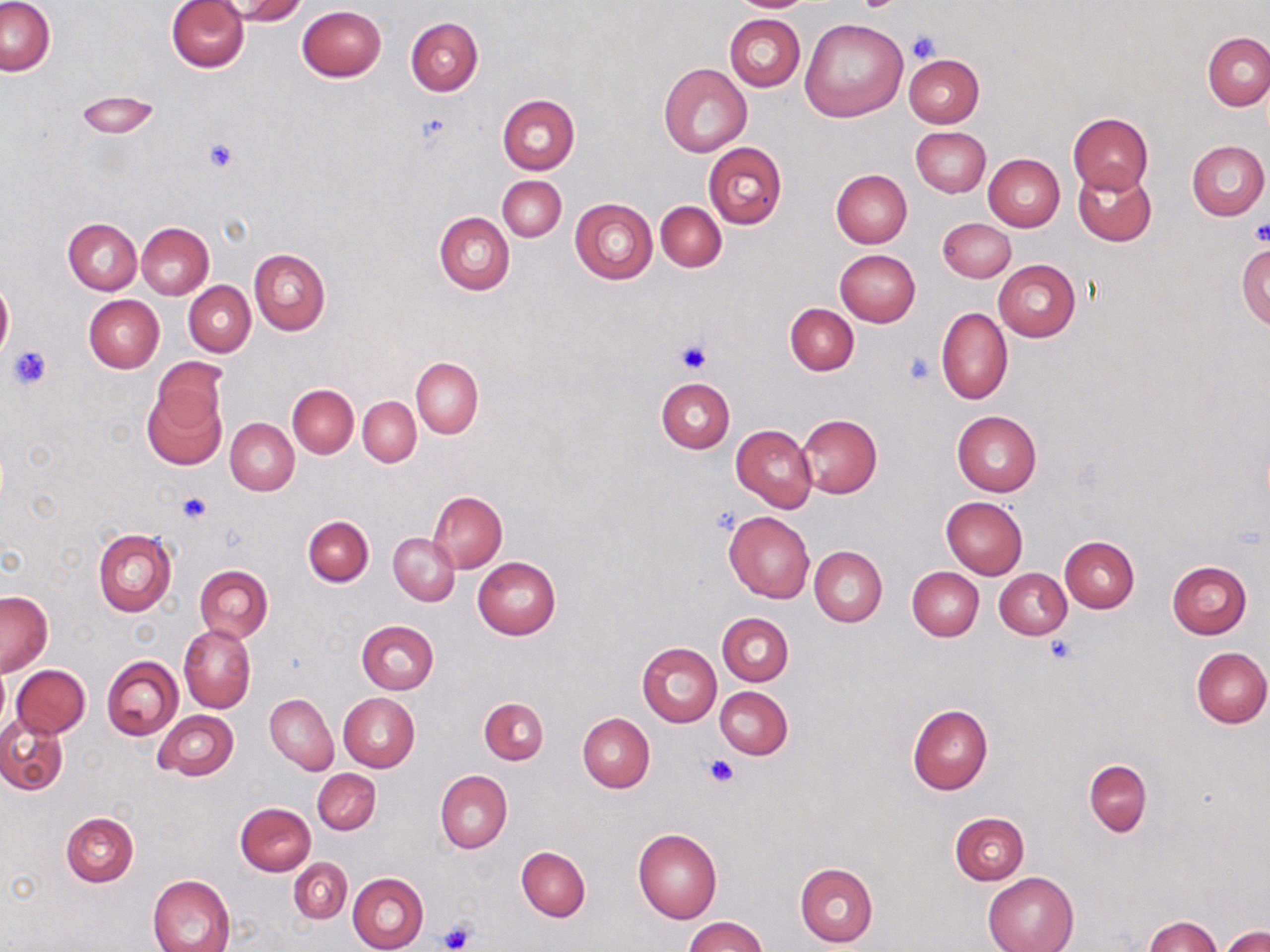
slide-level diagnosis = no evidence of blood parasites
stain = May-Grünwald-Giemsa
platelet locations = approximate bounding boxes as named x1/y1/x2/y2 corners in pixels: (x1=854, y1=0, x2=900, y2=12), (x1=908, y1=30, x2=938, y2=63), (x1=415, y1=111, x2=454, y2=148), (x1=204, y1=138, x2=238, y2=173), (x1=1249, y1=222, x2=1270, y2=248), (x1=675, y1=340, x2=712, y2=375), (x1=7, y1=345, x2=52, y2=391), (x1=903, y1=352, x2=936, y2=386), (x1=177, y1=491, x2=212, y2=526), (x1=1045, y1=636, x2=1078, y2=664), (x1=705, y1=756, x2=738, y2=788), (x1=438, y1=923, x2=476, y2=951)
modality = optical microscopy
uninfected red blood cell locations = approximate bounding boxes as named x1/y1/x2/y2 corners in pixels: (x1=167, y1=0, x2=249, y2=72), (x1=227, y1=0, x2=306, y2=24), (x1=730, y1=0, x2=814, y2=11), (x1=1, y1=1, x2=55, y2=76), (x1=298, y1=5, x2=387, y2=81), (x1=726, y1=14, x2=805, y2=90), (x1=405, y1=17, x2=482, y2=95), (x1=799, y1=17, x2=907, y2=122), (x1=1203, y1=32, x2=1270, y2=111), (x1=903, y1=53, x2=984, y2=127), (x1=658, y1=63, x2=751, y2=156), (x1=75, y1=90, x2=161, y2=139), (x1=496, y1=94, x2=580, y2=174), (x1=1069, y1=113, x2=1153, y2=194), (x1=910, y1=127, x2=989, y2=197), (x1=1186, y1=140, x2=1268, y2=220), (x1=703, y1=142, x2=786, y2=229), (x1=984, y1=154, x2=1064, y2=231), (x1=1073, y1=168, x2=1156, y2=247), (x1=831, y1=169, x2=912, y2=248), (x1=498, y1=176, x2=565, y2=242), (x1=570, y1=199, x2=658, y2=284), (x1=656, y1=202, x2=726, y2=270), (x1=434, y1=211, x2=514, y2=295), (x1=64, y1=218, x2=141, y2=295), (x1=938, y1=218, x2=1015, y2=281), (x1=136, y1=223, x2=213, y2=299), (x1=1238, y1=244, x2=1270, y2=327), (x1=250, y1=248, x2=330, y2=335), (x1=834, y1=249, x2=919, y2=328), (x1=993, y1=259, x2=1080, y2=341), (x1=0, y1=280, x2=13, y2=357), (x1=184, y1=282, x2=255, y2=356), (x1=83, y1=295, x2=164, y2=373), (x1=785, y1=304, x2=858, y2=375), (x1=936, y1=307, x2=1012, y2=405), (x1=412, y1=358, x2=482, y2=438), (x1=144, y1=374, x2=227, y2=467), (x1=655, y1=378, x2=734, y2=453), (x1=287, y1=384, x2=359, y2=458), (x1=358, y1=397, x2=420, y2=467), (x1=952, y1=411, x2=1041, y2=496), (x1=796, y1=414, x2=882, y2=498), (x1=226, y1=418, x2=299, y2=495), (x1=732, y1=425, x2=816, y2=512), (x1=428, y1=491, x2=506, y2=572), (x1=941, y1=496, x2=1029, y2=579), (x1=724, y1=511, x2=814, y2=603), (x1=303, y1=515, x2=373, y2=586), (x1=93, y1=529, x2=176, y2=616), (x1=388, y1=533, x2=459, y2=605), (x1=1060, y1=536, x2=1139, y2=613), (x1=810, y1=546, x2=887, y2=627), (x1=473, y1=557, x2=561, y2=639), (x1=1168, y1=561, x2=1253, y2=639), (x1=194, y1=565, x2=273, y2=642), (x1=907, y1=566, x2=984, y2=641), (x1=995, y1=568, x2=1071, y2=638), (x1=0, y1=591, x2=52, y2=677), (x1=718, y1=612, x2=793, y2=686), (x1=357, y1=620, x2=438, y2=694), (x1=179, y1=624, x2=255, y2=714), (x1=637, y1=642, x2=722, y2=727), (x1=1191, y1=646, x2=1270, y2=727), (x1=102, y1=656, x2=183, y2=739), (x1=11, y1=665, x2=90, y2=738), (x1=0, y1=667, x2=10, y2=735), (x1=715, y1=687, x2=793, y2=760), (x1=265, y1=693, x2=338, y2=775), (x1=338, y1=693, x2=419, y2=772), (x1=479, y1=697, x2=548, y2=763), (x1=907, y1=705, x2=992, y2=795), (x1=153, y1=710, x2=238, y2=781), (x1=577, y1=713, x2=654, y2=792), (x1=1, y1=714, x2=68, y2=794), (x1=1083, y1=759, x2=1152, y2=837), (x1=312, y1=769, x2=380, y2=835), (x1=434, y1=771, x2=511, y2=853), (x1=236, y1=802, x2=316, y2=876), (x1=61, y1=812, x2=138, y2=886), (x1=950, y1=813, x2=1028, y2=884), (x1=633, y1=828, x2=722, y2=923), (x1=516, y1=846, x2=589, y2=920), (x1=289, y1=857, x2=351, y2=924), (x1=795, y1=862, x2=878, y2=948), (x1=347, y1=872, x2=429, y2=952), (x1=982, y1=872, x2=1079, y2=952), (x1=148, y1=874, x2=235, y2=952), (x1=1144, y1=915, x2=1222, y2=951), (x1=683, y1=916, x2=767, y2=952), (x1=1221, y1=926, x2=1269, y2=952)
preparation = thin blood film
field of view = one of a larger specimen
image size = 1270×952 pixels
magnification = 1000x